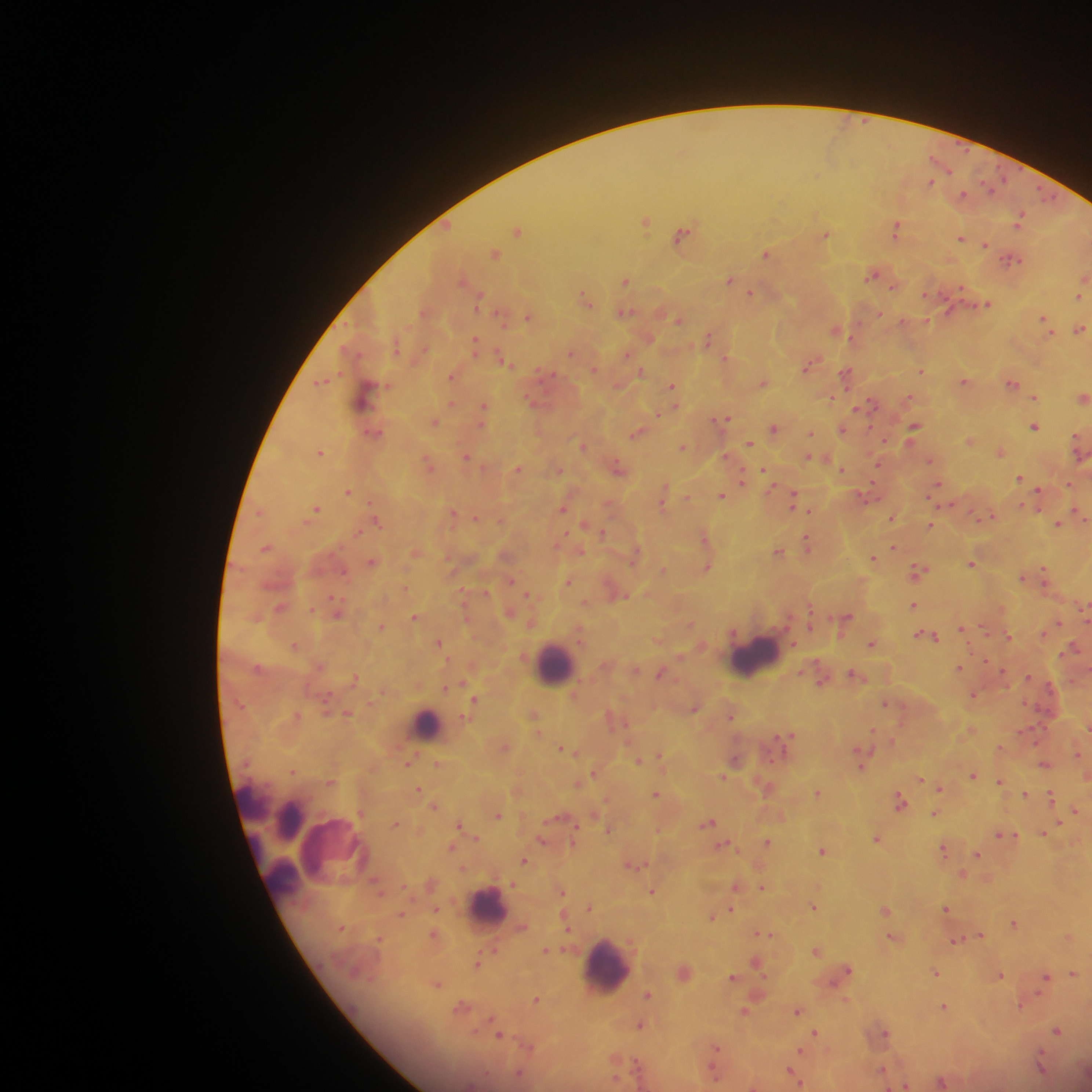
Approximate centers as x y in pixels.
Summary:
  - Plasmodium parasite locations: 930 181; 963 194; 646 221; 1019 221; 896 229; 518 230; 683 234; 826 234; 961 238; 985 245; 494 253; 765 253; 1009 259; 872 275; 626 280; 729 280; 750 293; 1079 296; 585 297; 479 299; 986 304; 623 312; 528 317; 679 319; 1045 322; 1080 329; 836 331; 708 338; 475 342; 571 352; 627 353; 502 358; 808 365; 594 369; 921 370; 642 372; 546 374; 846 374; 451 376; 322 381; 964 381; 763 383; 1011 383; 672 386; 364 395; 1034 397; 830 398; 1083 398; 872 404; 484 406; 723 418; 436 422; 914 427; 1034 427; 774 428; 842 429; 374 433; 811 433; 636 434; 970 440; 1077 442; 749 444; 583 446; 683 447; 320 452; 1000 452; 465 456; 809 456; 930 461; 428 463; 617 467; 519 469; 842 469; 558 470; 766 471; 744 476; 1020 478; 937 486; 1039 491; 348 492; 866 495; 722 496; 793 499; 662 503; 315 509; 563 509; 1079 512; 453 514; 989 516; 475 517; 892 518; 376 521; 1058 523; 929 525; 602 532; 807 542; 265 547; 893 547; 581 551; 778 552; 874 558; 372 563; 971 563; 708 567; 662 570; 918 571; 1044 573; 1022 576; 511 581; 568 581; 528 594; 625 596; 913 605; 280 607; 311 609; 415 617; 847 618; 1057 622; 382 626; 962 629; 929 636; 1009 636; 439 643; 294 644; 872 644; 1074 646; 959 668; 1001 671; 660 673; 855 675; 355 679; 445 688; 973 695; 475 700; 886 702; 695 708; 348 713; 730 715; 1087 727; 873 731; 788 736; 504 747; 563 749; 1079 755; 661 756; 735 759; 861 760; 639 761; 408 762; 437 763; 1044 765; 293 771; 594 772; 973 775; 723 777; 922 779; 1000 782; 766 787; 941 788; 418 789; 817 793; 656 794; 1025 795; 1051 797; 900 801; 434 806; 1075 811; 935 813; 498 815; 708 823; 395 824; 458 825; 608 830; 1044 833; 1003 834; 541 839; 876 839; 767 842; 725 844; 943 849; 823 851; 976 854; 524 860; 631 865; 962 874; 736 885; 762 887; 652 891; 562 892; 813 906; 589 907; 946 908; 436 909; 731 909; 886 911; 401 914; 712 917; 1014 924; 764 934; 981 936; 892 938; 955 940; 546 950; 817 951; 758 962; 477 964; 846 970; 936 973; 1074 973; 1000 975; 733 977; 1044 978; 437 984; 648 994; 536 1000; 1021 1005; 460 1007; 944 1007; 745 1011; 797 1011; 640 1026; 1057 1030; 815 1032; 884 1033; 499 1036; 715 1050; 1040 1066; 881 1070; 791 1072; 795 1078; 941 1082; 906 1085
  - Leukocyte locations: 754 657; 555 663; 425 725; 274 840; 487 905; 605 967
  - Field of view: single
  - Country: Ghana
  - Preparation: thick blood film
  - Image size: 1092×1092 pixels
  - Capture: mobile-phone photograph through a microscope